Report the malaria status of this cell.
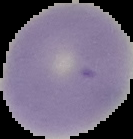
It is uninfected.

Cell region segmented out of the field of view; the surrounding area is masked to black. From a thin blood film. Image is 133×139 pixels.